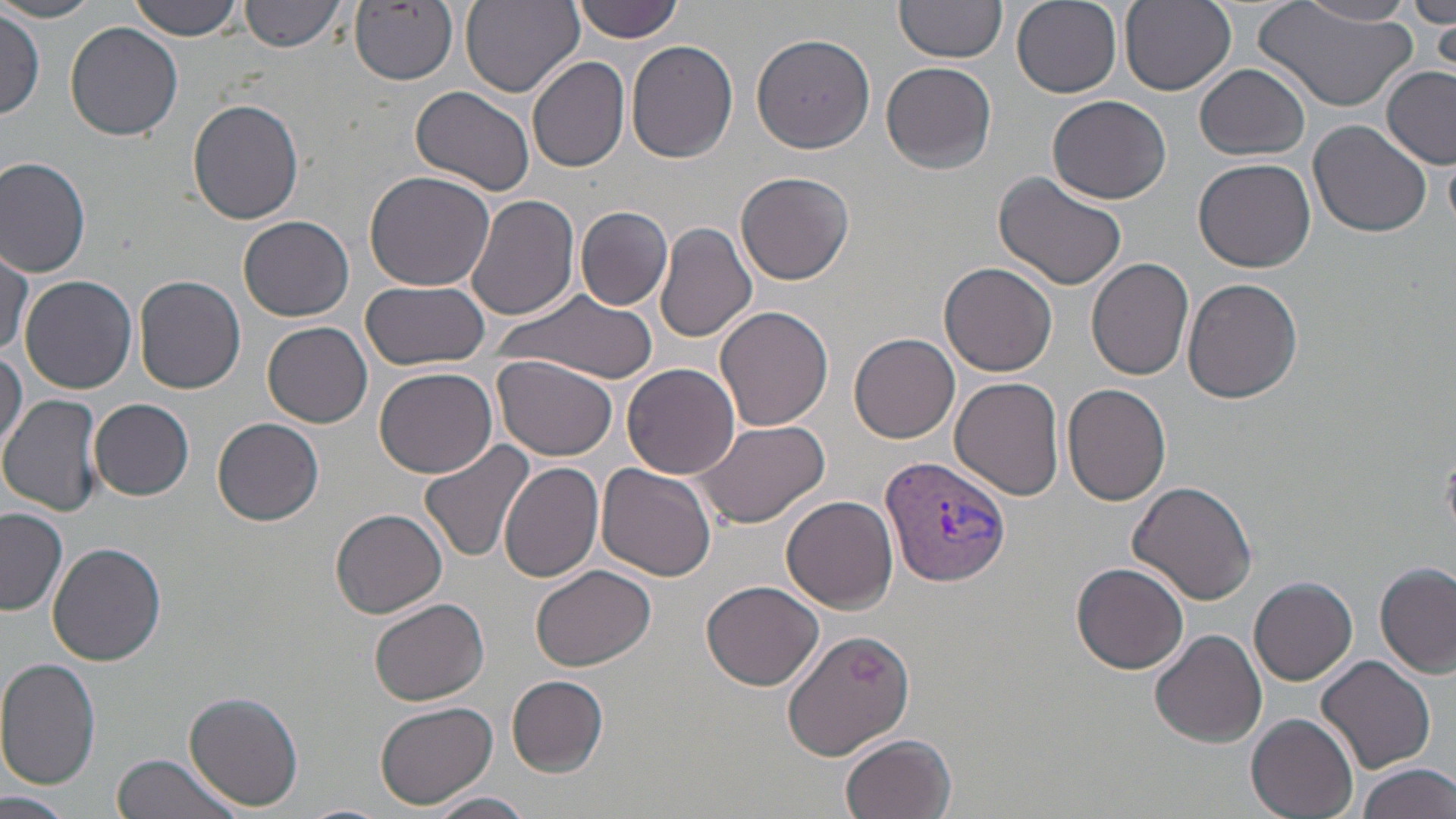

slide-level diagnosis = Plasmodium vivax
image size = 1456×819 pixels
stain = May-Grünwald-Giemsa
modality = optical microscopy
uninfected red blood cell locations = approximate bounding boxes as named x1/y1/x2/y2 corners in pixels: (x1=124, y1=0, x2=248, y2=40), (x1=239, y1=0, x2=348, y2=52), (x1=460, y1=0, x2=583, y2=97), (x1=1011, y1=0, x2=1122, y2=97), (x1=1119, y1=0, x2=1236, y2=94), (x1=1412, y1=0, x2=1456, y2=29), (x1=351, y1=1, x2=459, y2=87), (x1=571, y1=1, x2=687, y2=42), (x1=894, y1=1, x2=1009, y2=67), (x1=1296, y1=1, x2=1418, y2=27), (x1=0, y1=2, x2=105, y2=23), (x1=1256, y1=4, x2=1416, y2=112), (x1=2, y1=10, x2=41, y2=118), (x1=1427, y1=16, x2=1455, y2=73), (x1=65, y1=23, x2=183, y2=141), (x1=750, y1=30, x2=876, y2=152), (x1=626, y1=42, x2=738, y2=165), (x1=528, y1=56, x2=630, y2=172), (x1=881, y1=62, x2=997, y2=175), (x1=1195, y1=65, x2=1310, y2=161), (x1=1381, y1=68, x2=1455, y2=162), (x1=412, y1=85, x2=535, y2=198), (x1=1047, y1=94, x2=1173, y2=204), (x1=188, y1=99, x2=305, y2=225), (x1=1309, y1=119, x2=1433, y2=238), (x1=1444, y1=154, x2=1456, y2=230), (x1=0, y1=155, x2=94, y2=277), (x1=1194, y1=158, x2=1316, y2=274), (x1=364, y1=169, x2=496, y2=291), (x1=994, y1=170, x2=1131, y2=293), (x1=736, y1=171, x2=855, y2=285), (x1=465, y1=193, x2=579, y2=322), (x1=575, y1=205, x2=673, y2=311), (x1=238, y1=215, x2=355, y2=323), (x1=653, y1=222, x2=757, y2=345), (x1=1, y1=246, x2=32, y2=361), (x1=1085, y1=258, x2=1194, y2=382), (x1=939, y1=262, x2=1057, y2=376), (x1=134, y1=273, x2=247, y2=394), (x1=19, y1=275, x2=137, y2=393), (x1=1183, y1=278, x2=1305, y2=405), (x1=361, y1=279, x2=491, y2=370), (x1=498, y1=290, x2=660, y2=386), (x1=715, y1=302, x2=834, y2=431), (x1=263, y1=321, x2=373, y2=427), (x1=850, y1=332, x2=960, y2=443), (x1=0, y1=351, x2=24, y2=460), (x1=491, y1=354, x2=621, y2=459), (x1=622, y1=363, x2=740, y2=479), (x1=375, y1=365, x2=497, y2=478), (x1=950, y1=376, x2=1067, y2=500), (x1=1062, y1=383, x2=1172, y2=505), (x1=3, y1=394, x2=109, y2=516), (x1=91, y1=399, x2=194, y2=500), (x1=212, y1=416, x2=325, y2=527), (x1=691, y1=418, x2=830, y2=530), (x1=420, y1=440, x2=536, y2=560), (x1=499, y1=462, x2=605, y2=585), (x1=596, y1=464, x2=717, y2=581), (x1=1128, y1=480, x2=1259, y2=605), (x1=781, y1=495, x2=898, y2=613), (x1=0, y1=508, x2=68, y2=616), (x1=331, y1=508, x2=448, y2=619), (x1=47, y1=541, x2=167, y2=665), (x1=1071, y1=563, x2=1189, y2=676), (x1=532, y1=564, x2=654, y2=671), (x1=1375, y1=564, x2=1454, y2=677), (x1=1250, y1=576, x2=1358, y2=685), (x1=700, y1=580, x2=823, y2=691), (x1=370, y1=597, x2=490, y2=707), (x1=779, y1=626, x2=915, y2=760), (x1=1150, y1=628, x2=1267, y2=747), (x1=1317, y1=654, x2=1436, y2=773), (x1=0, y1=656, x2=101, y2=790), (x1=507, y1=675, x2=609, y2=776), (x1=186, y1=691, x2=302, y2=808), (x1=375, y1=700, x2=497, y2=809), (x1=1247, y1=714, x2=1359, y2=818), (x1=840, y1=732, x2=958, y2=819), (x1=110, y1=753, x2=245, y2=819), (x1=1356, y1=761, x2=1456, y2=819), (x1=0, y1=790, x2=69, y2=819), (x1=427, y1=791, x2=538, y2=819), (x1=293, y1=803, x2=392, y2=819)
magnification = 1000x
preparation = thin blood film
field of view = one of a larger specimen
Plasmodium vivax-infected red blood cell locations = approximate bounding boxes as named x1/y1/x2/y2 corners in pixels: (x1=882, y1=452, x2=1012, y2=588)